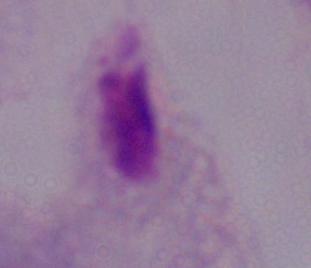

Summary:
  - Magnification: 1000x
  - Identification: trichomonad
  - Modality: photomicrograph